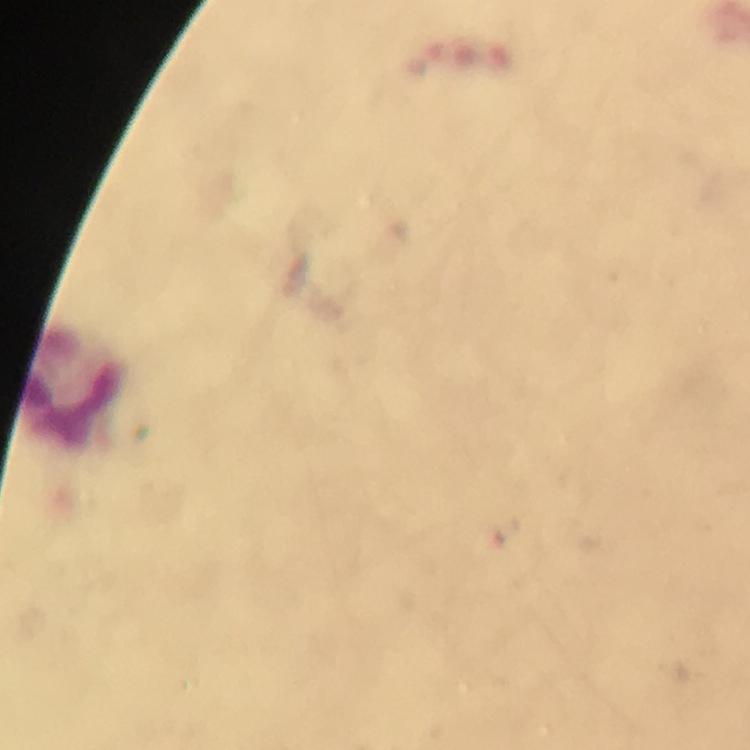
capture: smartphone mounted on the microscope
cropped_from: one field of view
magnification: 100x
leukocyte_locations: 'approximate centers as {x, y} in pixels: {77, 388}'
context: from a diagnostic examination for malaria
stain: Giemsa
image_size: 750×750 pixels
preparation: thick blood film
immersion_oil: applied
malaria_parasites: none seen